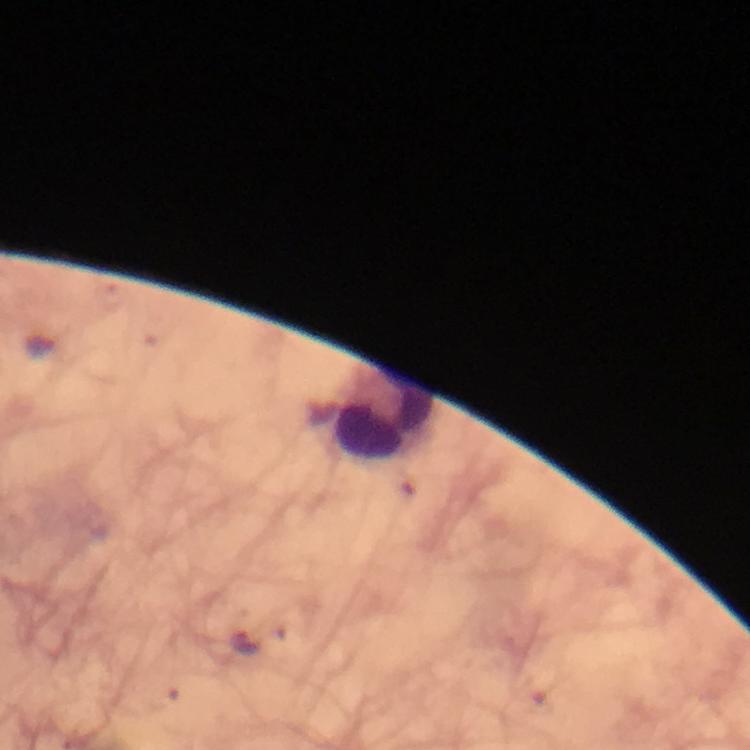
Approximate object centers, in pixels from the top-left corner. Leukocyte locations: (x=383, y=413). Malaria parasite locations: (x=245, y=643). Immersion oil was used. Image is 750×750 pixels. From a diagnostic examination for malaria. Giemsa stain. Thick blood smear. Smartphone photograph taken through a microscope. At 100x magnification. A crop from one field of view.